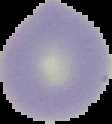 Segmented cell region on a black background. From a thin blood film. Image is 112×124 pixels. Malaria status: uninfected.